Comment on the morphology of the red blood cells.
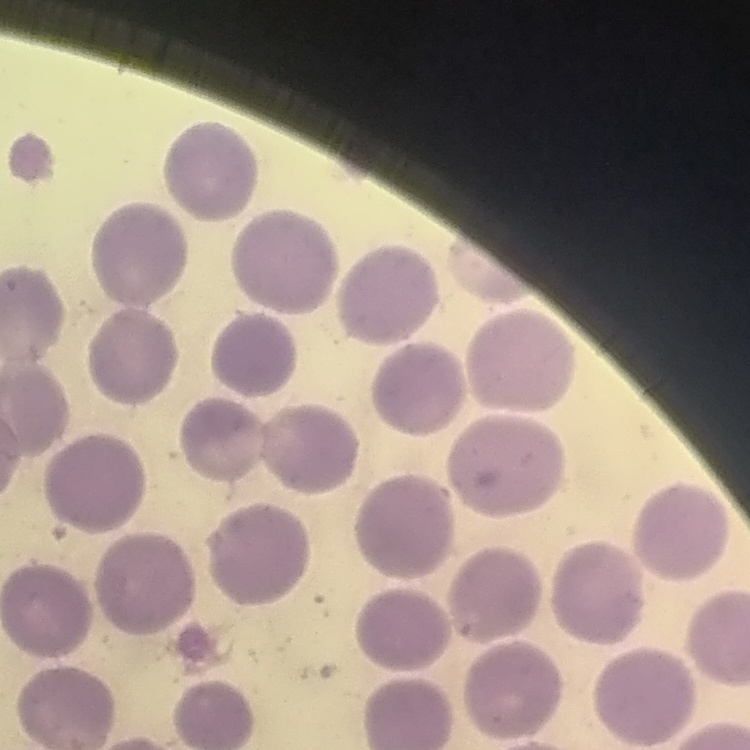

They show no rouleaux formation.

Summary:
  - Preparation: thin blood smear
  - Stain: Field's or Giemsa
  - Image type: square crop of a larger photomicrograph